State which cell type is depicted.
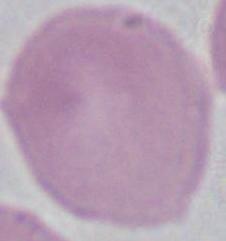

An erythrocyte.

modality = photomicrograph
magnification = 1000x